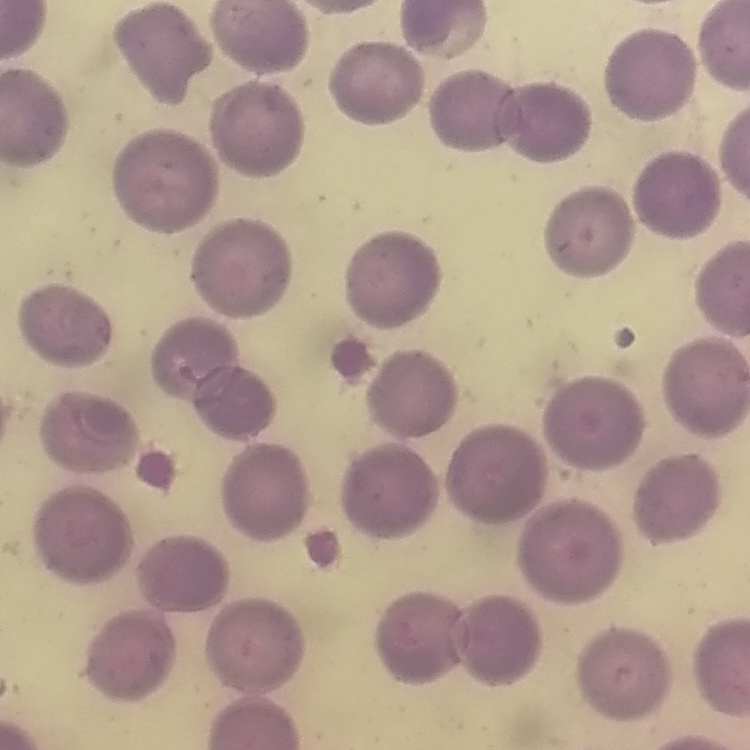

Summary:
  - Red blood cell morphology: no rouleaux formation
  - Preparation: thin blood smear
  - Image type: one tile cut from a larger photomicrograph
  - Stain: Field's or Giemsa